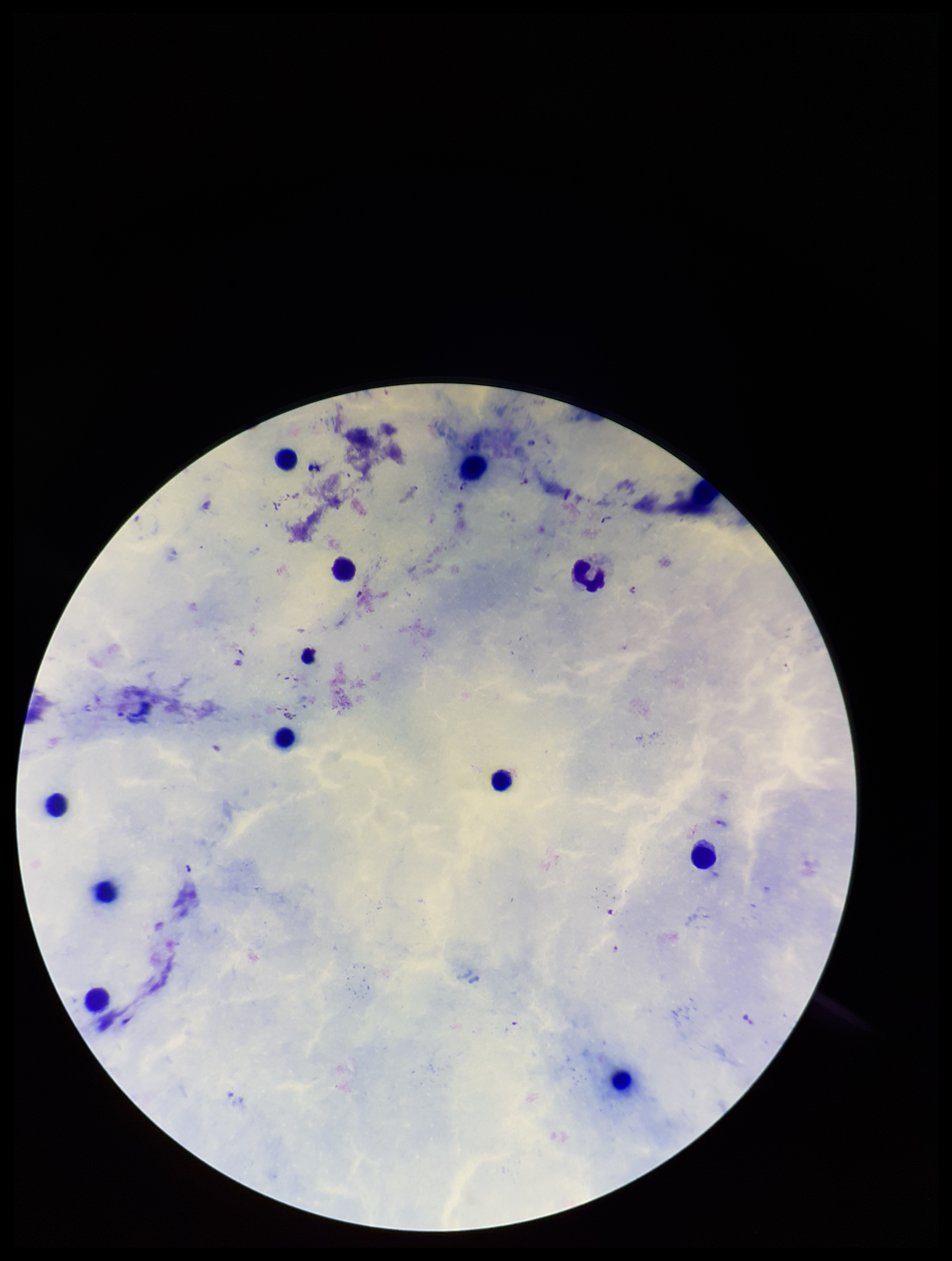 Leukocyte count: 12. Parasite count: 2. Species reported for this patient: Plasmodium falciparum. One field from this slide. Patient malaria status: infected. Preparation: thick. Plasmodium parasites: seen. Smartphone photograph taken through the eyepiece of a microscope. Image is 952×1261 pixels. Stained with Giemsa.